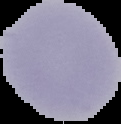

malaria status = uninfected
image size = 121×124 pixels
preparation = thin blood film
image type = segmented cell region on a black background